Describe the morphology of the erythrocytes.
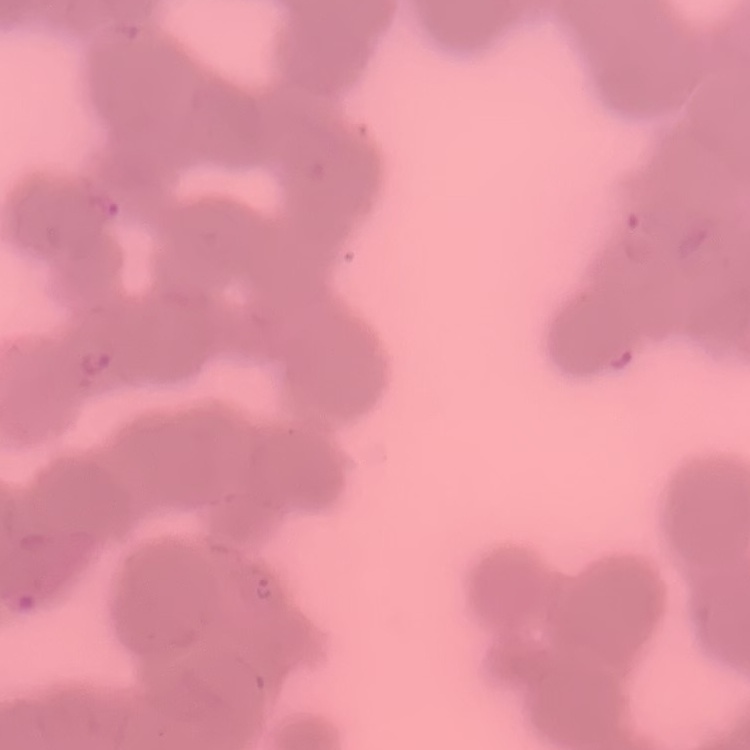
Rouleaux formation.

{
  "image_type": "one tile cut from a larger photomicrograph",
  "stain": "Field's or Giemsa",
  "preparation": "thin blood smear"
}